State the blood parasite species.
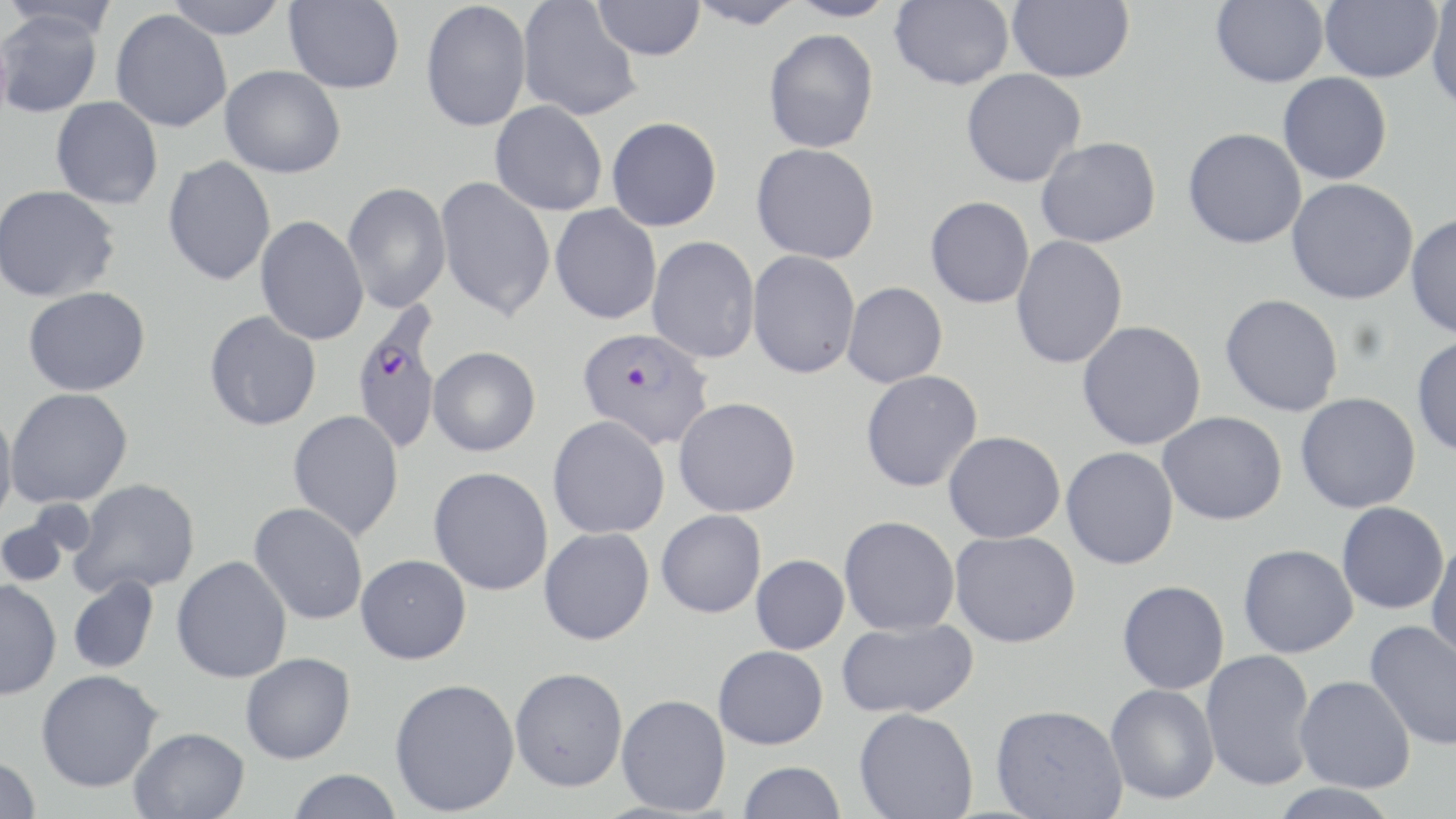

Plasmodium falciparum.

Summary:
  - Coordinate format: approximate bounding boxes as named x1/y1/x2/y2 corners in pixels
  - Uninfected red blood cell locations: (x1=1, y1=0, x2=121, y2=40), (x1=162, y1=0, x2=289, y2=39), (x1=284, y1=0, x2=405, y2=93), (x1=517, y1=0, x2=642, y2=121), (x1=593, y1=0, x2=705, y2=60), (x1=685, y1=0, x2=806, y2=29), (x1=785, y1=0, x2=899, y2=22), (x1=890, y1=0, x2=1014, y2=90), (x1=1006, y1=0, x2=1135, y2=83), (x1=1211, y1=0, x2=1329, y2=87), (x1=1319, y1=0, x2=1442, y2=82), (x1=1426, y1=0, x2=1456, y2=112), (x1=420, y1=1, x2=532, y2=132), (x1=0, y1=9, x2=103, y2=118), (x1=110, y1=9, x2=232, y2=132), (x1=763, y1=29, x2=879, y2=153), (x1=220, y1=65, x2=346, y2=178), (x1=961, y1=68, x2=1087, y2=187), (x1=1277, y1=72, x2=1392, y2=185), (x1=51, y1=96, x2=164, y2=209), (x1=490, y1=101, x2=608, y2=216), (x1=606, y1=116, x2=722, y2=231), (x1=1182, y1=127, x2=1307, y2=249), (x1=1036, y1=136, x2=1161, y2=248), (x1=751, y1=142, x2=880, y2=264), (x1=163, y1=155, x2=276, y2=286), (x1=435, y1=175, x2=556, y2=321), (x1=1285, y1=178, x2=1419, y2=305), (x1=343, y1=182, x2=451, y2=312), (x1=0, y1=185, x2=121, y2=302), (x1=925, y1=196, x2=1035, y2=308), (x1=550, y1=204, x2=662, y2=324), (x1=1406, y1=212, x2=1456, y2=339), (x1=255, y1=215, x2=369, y2=345), (x1=1011, y1=235, x2=1128, y2=369), (x1=647, y1=236, x2=760, y2=364), (x1=747, y1=250, x2=861, y2=378), (x1=842, y1=282, x2=948, y2=388), (x1=23, y1=286, x2=151, y2=396), (x1=1220, y1=293, x2=1343, y2=417), (x1=204, y1=310, x2=322, y2=431), (x1=1077, y1=320, x2=1207, y2=450), (x1=1412, y1=335, x2=1456, y2=458), (x1=428, y1=346, x2=541, y2=456), (x1=860, y1=370, x2=983, y2=492), (x1=5, y1=387, x2=132, y2=507), (x1=1295, y1=392, x2=1421, y2=513), (x1=674, y1=397, x2=801, y2=517), (x1=0, y1=409, x2=18, y2=524), (x1=288, y1=409, x2=404, y2=541), (x1=1158, y1=411, x2=1287, y2=525), (x1=548, y1=415, x2=671, y2=538), (x1=943, y1=431, x2=1066, y2=543), (x1=1061, y1=446, x2=1179, y2=569), (x1=429, y1=467, x2=553, y2=595), (x1=70, y1=478, x2=201, y2=597), (x1=249, y1=502, x2=368, y2=625), (x1=1336, y1=502, x2=1449, y2=614), (x1=656, y1=509, x2=767, y2=617), (x1=838, y1=515, x2=960, y2=636), (x1=0, y1=517, x2=71, y2=587), (x1=539, y1=527, x2=654, y2=645), (x1=950, y1=530, x2=1081, y2=647), (x1=1426, y1=538, x2=1456, y2=664), (x1=1238, y1=544, x2=1358, y2=658), (x1=356, y1=554, x2=471, y2=664), (x1=750, y1=554, x2=850, y2=654), (x1=172, y1=555, x2=292, y2=683), (x1=68, y1=576, x2=158, y2=674), (x1=0, y1=579, x2=62, y2=700), (x1=1117, y1=580, x2=1230, y2=695), (x1=836, y1=618, x2=978, y2=719), (x1=1364, y1=620, x2=1456, y2=751), (x1=713, y1=645, x2=829, y2=750), (x1=1201, y1=649, x2=1317, y2=791), (x1=240, y1=652, x2=355, y2=764), (x1=510, y1=666, x2=628, y2=791), (x1=36, y1=669, x2=162, y2=792), (x1=1294, y1=675, x2=1416, y2=793), (x1=389, y1=677, x2=520, y2=816), (x1=1105, y1=684, x2=1220, y2=805), (x1=616, y1=693, x2=731, y2=815), (x1=990, y1=704, x2=1128, y2=819), (x1=854, y1=707, x2=978, y2=819), (x1=129, y1=727, x2=250, y2=819), (x1=0, y1=756, x2=42, y2=818), (x1=737, y1=760, x2=847, y2=819), (x1=287, y1=769, x2=403, y2=819), (x1=1268, y1=782, x2=1402, y2=818)
  - Plasmodium falciparum-infected red blood cell locations: (x1=351, y1=305, x2=443, y2=457), (x1=577, y1=326, x2=714, y2=449)
  - Preparation: thin blood smear
  - Stain: May-Grünwald-Giemsa
  - Magnification: 1000x
  - Image size: 1456×819 pixels
  - Modality: light microscopy
  - Field of view: one of a larger specimen